Outline each blood parasite and name the species.
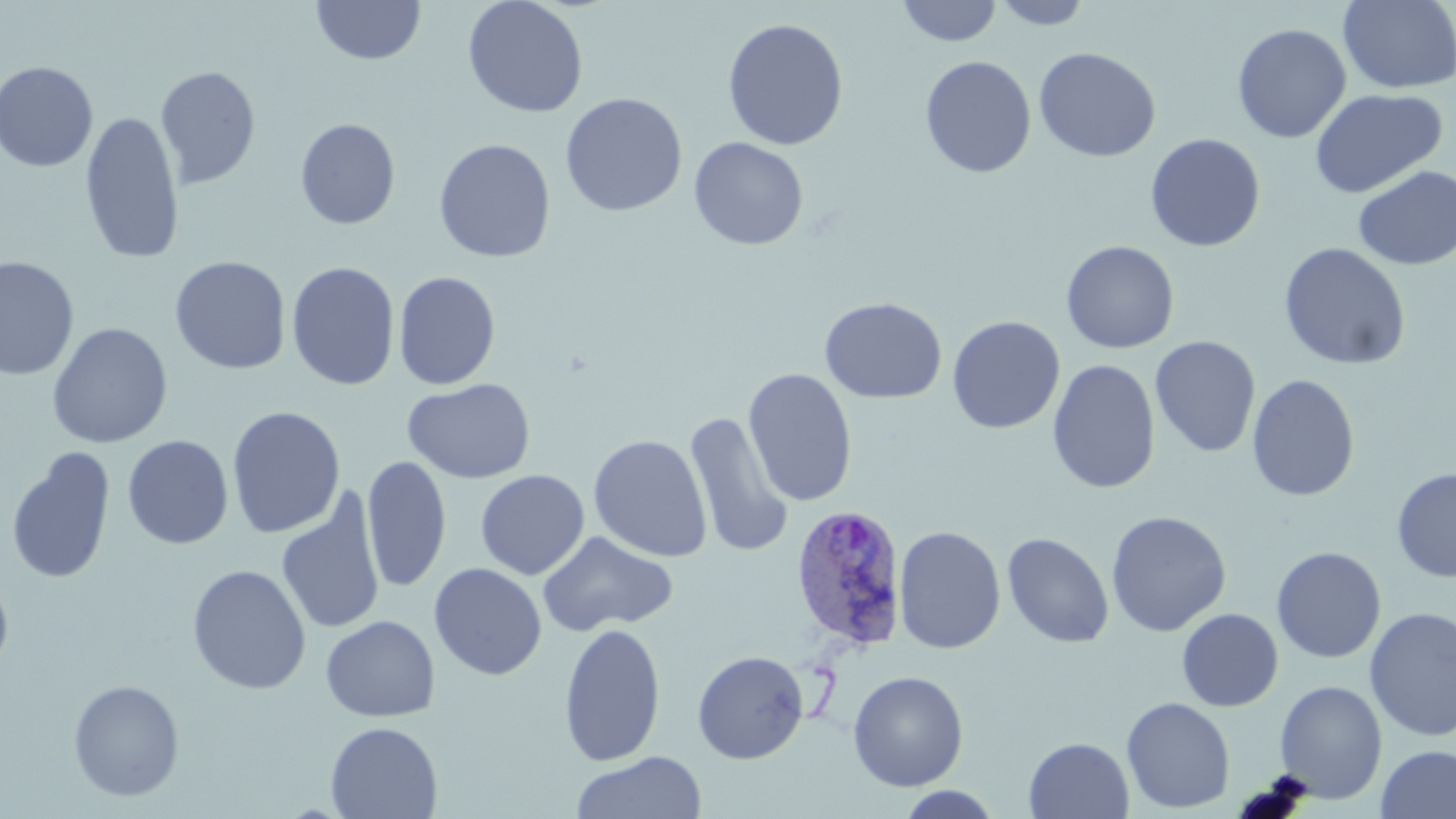
Approximate bounding boxes as named x1/y1/x2/y2 corners in pixels.
Plasmodium ovale-infected red blood cells: (x1=789, y1=503, x2=910, y2=653).
No Plasmodium falciparum, Plasmodium malariae, Plasmodium vivax, Babesia divergens, or Trypanosoma brucei observed.

Summary:
  - Uninfected red blood cell locations: (x1=311, y1=0, x2=426, y2=65), (x1=462, y1=0, x2=589, y2=118), (x1=896, y1=0, x2=1002, y2=47), (x1=991, y1=1, x2=1094, y2=30), (x1=1338, y1=1, x2=1455, y2=94), (x1=722, y1=18, x2=849, y2=151), (x1=1232, y1=24, x2=1352, y2=143), (x1=1034, y1=46, x2=1162, y2=162), (x1=920, y1=56, x2=1036, y2=178), (x1=0, y1=61, x2=99, y2=172), (x1=154, y1=65, x2=261, y2=190), (x1=1309, y1=88, x2=1448, y2=199), (x1=560, y1=93, x2=687, y2=217), (x1=80, y1=110, x2=185, y2=264), (x1=295, y1=118, x2=400, y2=230), (x1=1145, y1=133, x2=1266, y2=253), (x1=689, y1=136, x2=809, y2=250), (x1=433, y1=138, x2=556, y2=263), (x1=1353, y1=165, x2=1456, y2=270), (x1=1061, y1=240, x2=1180, y2=354), (x1=1277, y1=242, x2=1412, y2=371), (x1=0, y1=256, x2=79, y2=381), (x1=170, y1=256, x2=292, y2=374), (x1=286, y1=261, x2=400, y2=391), (x1=393, y1=271, x2=501, y2=390), (x1=819, y1=297, x2=947, y2=404), (x1=947, y1=315, x2=1065, y2=434), (x1=47, y1=322, x2=173, y2=449), (x1=1150, y1=335, x2=1261, y2=458), (x1=1047, y1=359, x2=1161, y2=494), (x1=743, y1=368, x2=858, y2=507), (x1=1246, y1=374, x2=1360, y2=502), (x1=403, y1=378, x2=536, y2=484), (x1=226, y1=405, x2=346, y2=539), (x1=683, y1=411, x2=794, y2=558), (x1=588, y1=434, x2=713, y2=562), (x1=122, y1=435, x2=234, y2=550), (x1=7, y1=445, x2=235, y2=567), (x1=5, y1=447, x2=116, y2=585), (x1=362, y1=455, x2=451, y2=593), (x1=358, y1=462, x2=554, y2=586), (x1=1392, y1=467, x2=1456, y2=582), (x1=475, y1=469, x2=590, y2=580), (x1=276, y1=491, x2=386, y2=637), (x1=1105, y1=511, x2=1231, y2=637), (x1=893, y1=525, x2=1006, y2=654), (x1=537, y1=531, x2=679, y2=636), (x1=1002, y1=532, x2=1114, y2=648), (x1=1271, y1=546, x2=1387, y2=664), (x1=428, y1=563, x2=547, y2=680), (x1=187, y1=564, x2=311, y2=694), (x1=0, y1=570, x2=14, y2=677), (x1=1364, y1=607, x2=1456, y2=742), (x1=1177, y1=608, x2=1283, y2=711), (x1=321, y1=615, x2=440, y2=722), (x1=558, y1=622, x2=667, y2=767), (x1=692, y1=650, x2=809, y2=764), (x1=847, y1=670, x2=968, y2=791), (x1=67, y1=678, x2=185, y2=802), (x1=1274, y1=679, x2=1388, y2=804), (x1=1121, y1=696, x2=1236, y2=814), (x1=325, y1=721, x2=443, y2=819), (x1=1023, y1=736, x2=1134, y2=819), (x1=1376, y1=745, x2=1456, y2=819), (x1=571, y1=751, x2=707, y2=819), (x1=894, y1=786, x2=1004, y2=818)
  - Slide-level diagnosis: Plasmodium ovale
  - Modality: light microscopy
  - Field of view: one of a larger specimen
  - Preparation: thin blood smear
  - Image size: 1456×819 pixels
  - Stain: May-Grünwald-Giemsa
  - Magnification: 1000x